Assess this cell for malaria.
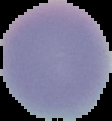

Uninfected.

image_size: 112×121 pixels
image_type: segmented cell region with the area outside set to black
preparation: thin blood film